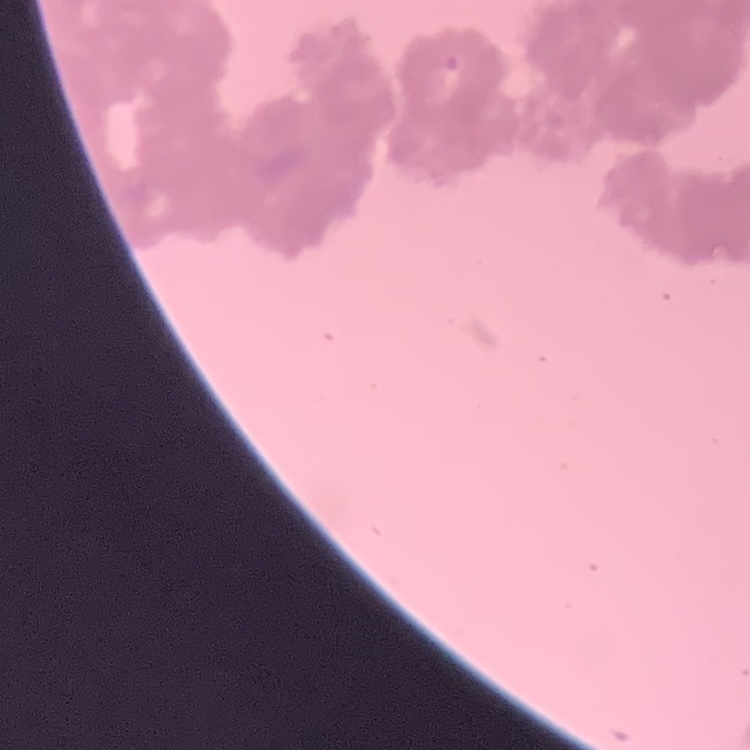

Summary:
  - Red blood cell morphology: rouleaux formation
  - Preparation: thin blood smear
  - Stain: Field's or Giemsa
  - Image type: one tile cut from a larger photomicrograph